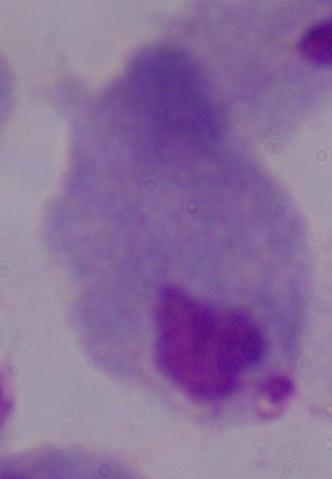
{
  "identification": "trichomonad",
  "magnification": "1000x",
  "modality": "micrograph"
}